Assess for Plasmodium parasites.
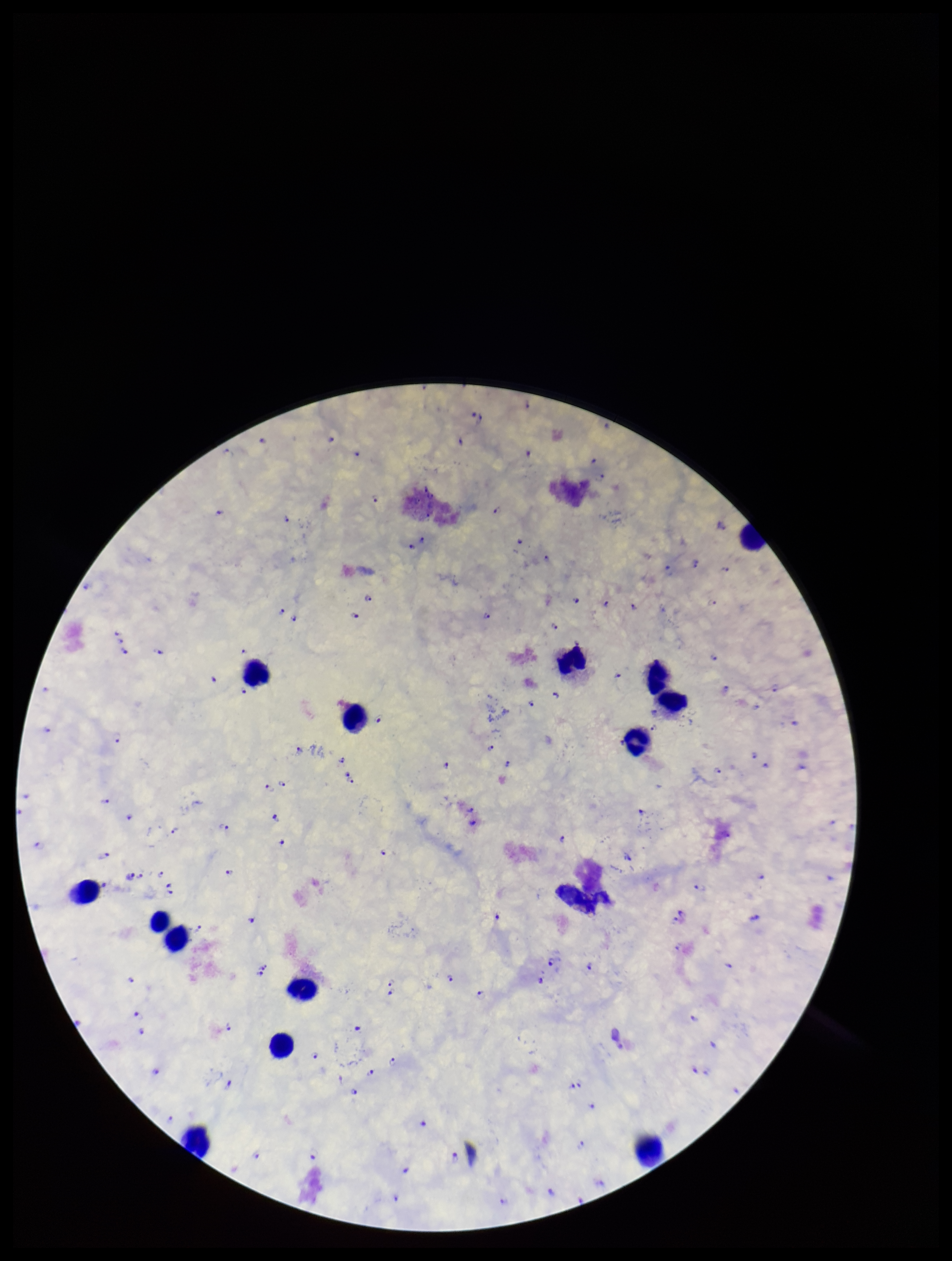
Identified.

{
  "species_reported_for_this_patient": "Plasmodium falciparum",
  "leukocyte_count": 14,
  "parasite_count": 111,
  "stain": "Giemsa",
  "patient_malaria_status": "infected",
  "preparation": "thick blood smear",
  "capture": "smartphone photograph through the microscope eyepiece",
  "field_of_view": "single",
  "image_size": "952×1261 pixels"
}